Report the malaria status of this cell.
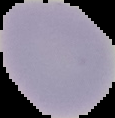

Uninfected.

preparation = thin blood film
image size = 115×118 pixels
image type = segmented cell region on a black background